Report the malaria status of this cell.
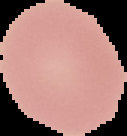
Uninfected.

Summary:
  - Image type: segmented cell region with the area outside set to black
  - Image size: 127×136 pixels
  - Preparation: thin blood smear